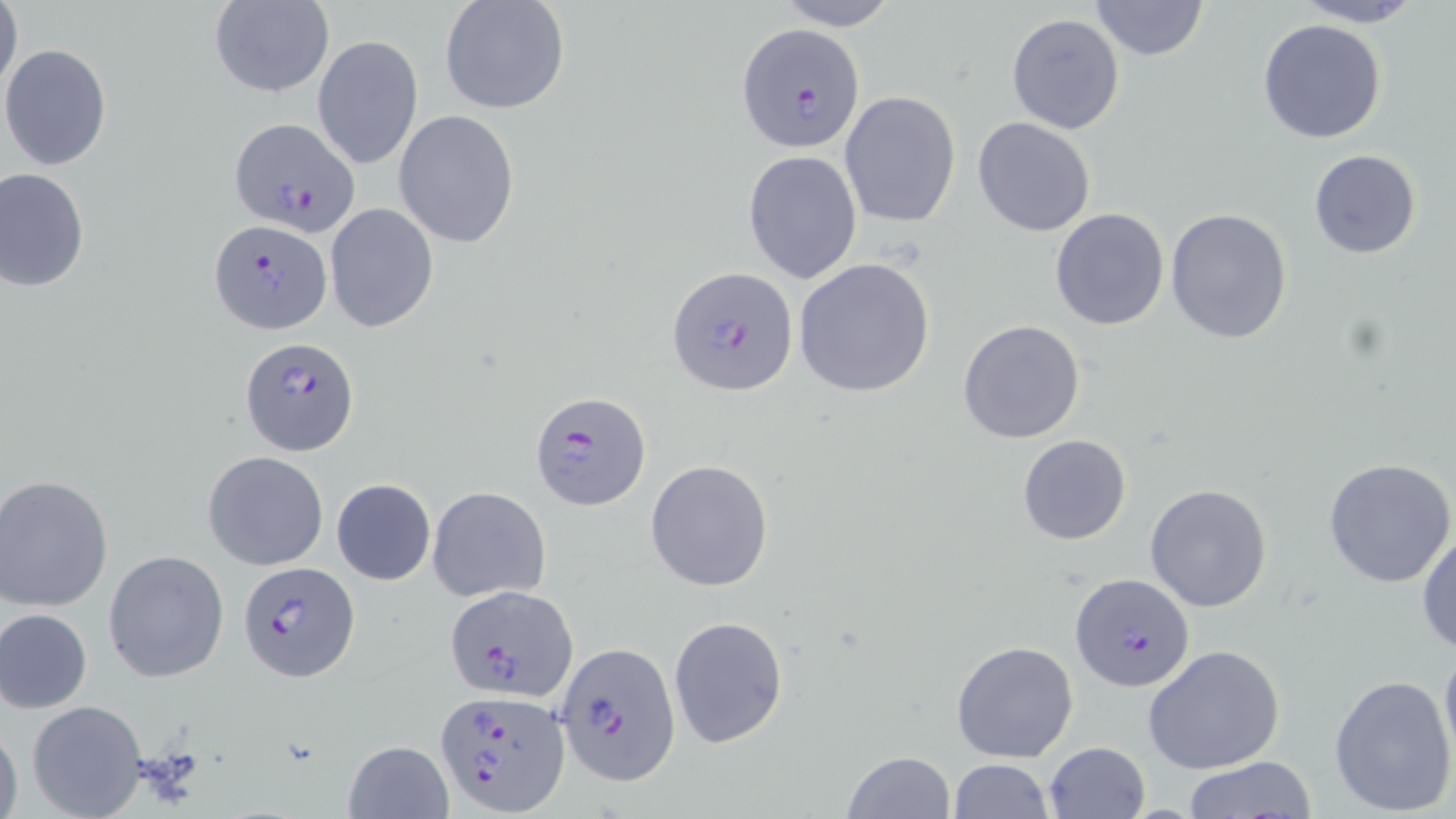

Summary:
  - Coordinate format: approximate bounding boxes as named x1/y1/x2/y2 corners in pixels
  - Plasmodium falciparum-infected red blood cell locations: (x1=738, y1=23, x2=865, y2=152), (x1=228, y1=117, x2=358, y2=238), (x1=209, y1=220, x2=332, y2=333), (x1=666, y1=265, x2=797, y2=395), (x1=239, y1=337, x2=358, y2=457), (x1=530, y1=390, x2=651, y2=510), (x1=236, y1=560, x2=358, y2=681), (x1=1070, y1=574, x2=1196, y2=693), (x1=443, y1=583, x2=578, y2=703), (x1=553, y1=642, x2=682, y2=786), (x1=437, y1=690, x2=568, y2=814)
  - Uninfected red blood cell locations: (x1=0, y1=0, x2=22, y2=103), (x1=439, y1=0, x2=571, y2=115), (x1=770, y1=0, x2=902, y2=30), (x1=1089, y1=0, x2=1210, y2=61), (x1=1293, y1=0, x2=1427, y2=27), (x1=208, y1=2, x2=333, y2=97), (x1=1006, y1=14, x2=1124, y2=134), (x1=1257, y1=19, x2=1388, y2=143), (x1=313, y1=34, x2=424, y2=171), (x1=1, y1=44, x2=114, y2=171), (x1=839, y1=91, x2=961, y2=228), (x1=394, y1=109, x2=521, y2=250), (x1=972, y1=117, x2=1096, y2=237), (x1=743, y1=149, x2=862, y2=286), (x1=1308, y1=149, x2=1423, y2=260), (x1=1, y1=167, x2=90, y2=290), (x1=324, y1=202, x2=439, y2=332), (x1=1049, y1=207, x2=1171, y2=331), (x1=1165, y1=209, x2=1293, y2=344), (x1=793, y1=257, x2=936, y2=398), (x1=957, y1=319, x2=1087, y2=444), (x1=1017, y1=434, x2=1132, y2=546), (x1=203, y1=451, x2=328, y2=570), (x1=1322, y1=458, x2=1456, y2=589), (x1=645, y1=459, x2=775, y2=592), (x1=2, y1=476, x2=116, y2=613), (x1=330, y1=477, x2=436, y2=585), (x1=1145, y1=484, x2=1272, y2=612), (x1=427, y1=486, x2=551, y2=604), (x1=1415, y1=526, x2=1456, y2=658), (x1=103, y1=549, x2=230, y2=685), (x1=1, y1=609, x2=93, y2=714), (x1=667, y1=615, x2=789, y2=750), (x1=1439, y1=637, x2=1456, y2=771), (x1=950, y1=640, x2=1078, y2=762), (x1=1143, y1=644, x2=1286, y2=775), (x1=1329, y1=673, x2=1456, y2=816), (x1=25, y1=700, x2=149, y2=818), (x1=0, y1=717, x2=22, y2=819), (x1=342, y1=739, x2=453, y2=817), (x1=1043, y1=741, x2=1152, y2=819), (x1=840, y1=750, x2=956, y2=818), (x1=949, y1=758, x2=1053, y2=818), (x1=1180, y1=758, x2=1319, y2=818)
  - Slide-level diagnosis: Plasmodium falciparum
  - Image size: 1456×819 pixels
  - Modality: optical microscopy
  - Preparation: thin blood smear
  - Field of view: single
  - Magnification: 1000x
  - Stain: May-Grünwald-Giemsa